Comment on the morphology of the red blood cells.
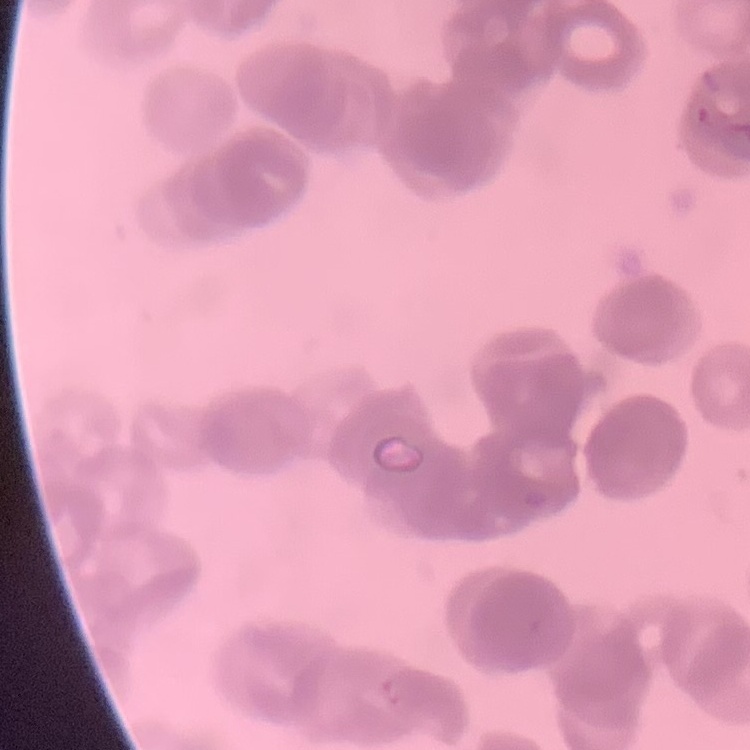

They show rouleaux formation.

One tile cut from a larger photomicrograph. Stained with either Field's or Giemsa. Thin blood film.